Identify the parasite.
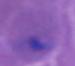

This is Plasmodium.

Summary:
  - Modality: photomicrograph
  - Magnification: 400x or 1000x